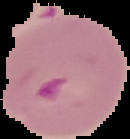
Image is 130×139 pixels. Malaria status: parasitized. Segmented cell region on a black background. From a thin blood smear.